Comment on the morphology of the red blood cells.
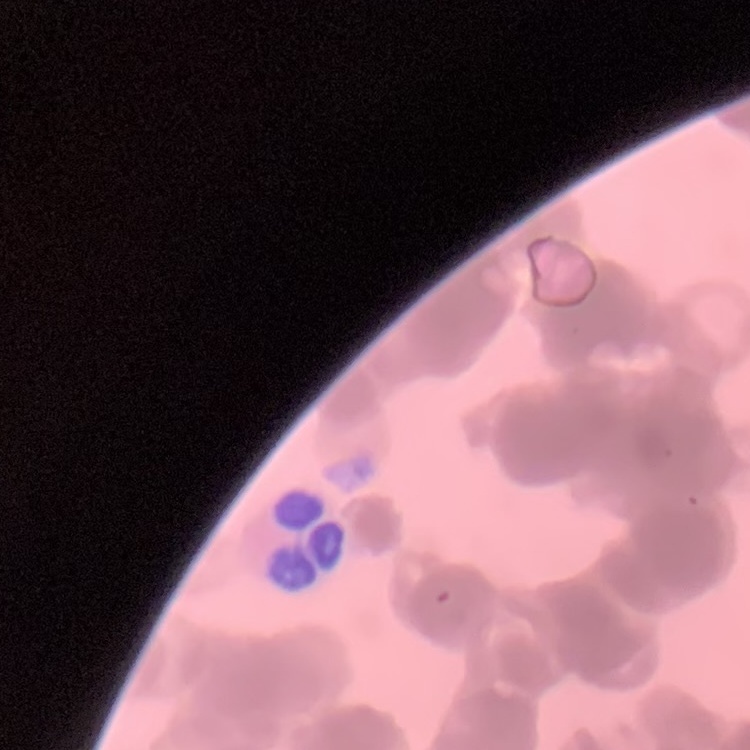
Rouleaux formation.

image type = one tile cut from a larger photomicrograph
preparation = thin blood film
stain = Field's or Giemsa